Assess this cell for malaria.
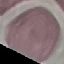
Uninfected.

Summary:
  - Capture: smartphone camera at the microscope eyepiece
  - Stain: Giemsa
  - Image type: cell patch, automatically extracted from a larger field of view and resized to 64 × 64 pixels
  - Preparation: thin blood smear